Assess this cell for malaria.
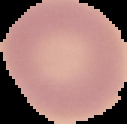

Uninfected.

image type = cell region segmented out of the field of view; surrounding area masked to black
preparation = thin blood smear
image size = 127×124 pixels